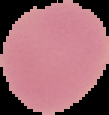
{
  "preparation": "thin blood film",
  "image_type": "segmented cell region on a black background",
  "result": "no Plasmodium parasites detected",
  "image_size": "109×115 pixels"
}